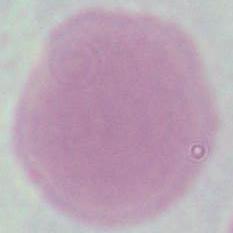

An erythrocyte is shown. Micrograph. Captured at 1000x magnification.